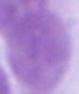
magnification = 1000x
modality = photomicrograph
identification = erythrocyte